Classify this cell by malaria status.
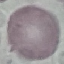
Uninfected.

{
  "capture": "smartphone through the microscope eyepiece",
  "stain": "Giemsa",
  "preparation": "thin smear",
  "image_type": "cell patch, automatically extracted from a larger field of view and resized to 64 × 64 pixels"
}